Assess this cell for malaria.
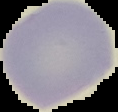
It is uninfected.

Image is 118×112 pixels. From a thin blood smear. Segmented cell region on a black background.